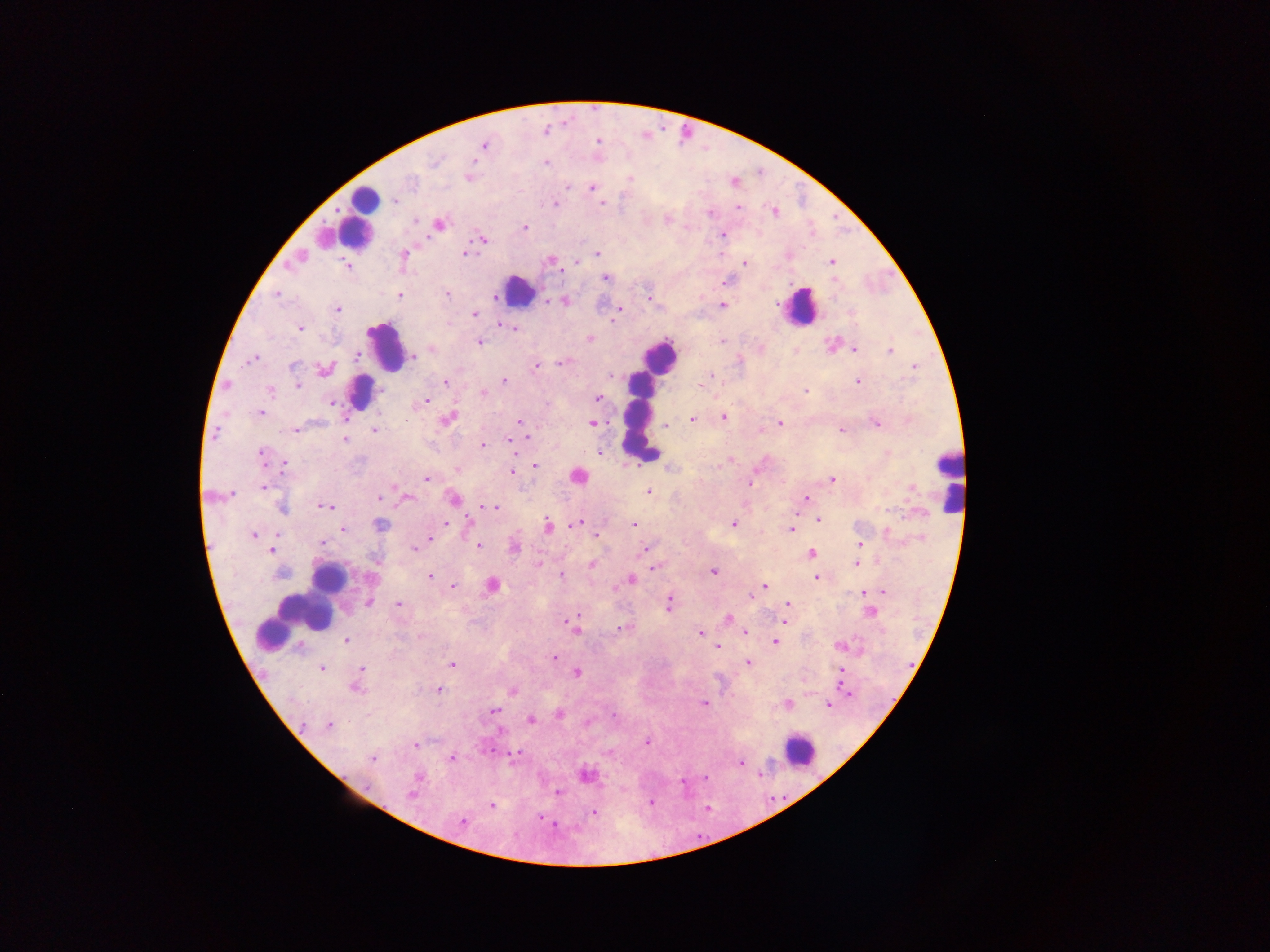
{
  "field_of_view": "single",
  "leukocyte_locations": "approximate centers as x y in pixels: 366 201; 358 218; 518 291; 799 307; 384 346; 659 356; 359 391; 639 415; 948 480; 328 579; 323 589; 300 613; 799 751",
  "preparation": "thick blood smear",
  "capture": "mobile-phone photograph through a microscope",
  "malaria_parasite_locations": "approximate centers as x y in pixels: 545 130; 597 140; 483 145; 545 163; 469 176; 630 178; 591 186; 393 199; 600 202; 555 204; 737 207; 773 211; 667 218; 438 224; 524 227; 722 234; 481 238; 464 253; 598 254; 403 255; 551 260; 295 261; 575 261; 832 262; 346 264; 744 264; 606 276; 727 281; 277 293; 447 294; 399 295; 647 297; 496 298; 565 300; 544 301; 723 305; 337 309; 619 309; 473 313; 614 316; 496 322; 501 324; 300 327; 513 327; 589 339; 722 341; 479 342; 830 345; 760 348; 432 349; 854 349; 795 351; 890 351; 356 354; 413 356; 252 358; 562 362; 535 366; 914 367; 324 369; 610 375; 504 380; 704 381; 858 381; 446 382; 297 385; 701 385; 227 386; 270 391; 805 391; 482 392; 597 397; 425 401; 330 402; 260 412; 724 417; 691 418; 447 419; 519 422; 875 422; 592 423; 665 423; 779 423; 295 429; 374 429; 841 430; 758 431; 526 438; 344 439; 508 440; 512 442; 481 445; 599 452; 261 454; 731 458; 284 463; 535 465; 670 467; 457 469; 512 472; 577 475; 427 478; 831 479; 749 483; 264 486; 647 491; 379 497; 407 497; 806 497; 453 499; 326 505; 282 507; 494 507; 817 519; 733 523; 577 524; 379 525; 633 525; 547 526; 343 529; 791 529; 254 534; 596 535; 430 538; 322 543; 860 544; 479 545; 514 548; 415 549; 644 549; 271 550; 810 553; 376 560; 539 564; 856 564; 592 565; 655 567; 713 571; 429 575; 560 576; 816 577; 630 580; 492 585; 452 586; 765 586; 614 589; 883 591; 862 593; 751 597; 368 602; 668 603; 787 604; 398 605; 869 612; 727 618; 783 621; 572 626; 620 628; 742 631; 700 632; 346 641; 775 641; 717 646; 840 646; 554 658; 747 662; 451 664; 321 668; 361 669; 840 671; 575 672; 355 687; 439 689; 511 691; 850 693; 704 704; 787 705; 828 705; 493 711; 558 714; 530 719; 588 722; 329 726; 498 729; 646 741; 415 745; 608 752; 514 754; 372 757; 452 758; 740 762; 586 774; 417 776; 704 778; 682 782; 558 792; 411 794; 651 803; 491 805; 594 812; 541 818; 462 821",
  "image_size": "1270×952 pixels",
  "country": "Ghana"
}